Give the position of every Plasmodium falciparum parasite, noting its life-cycle stage.
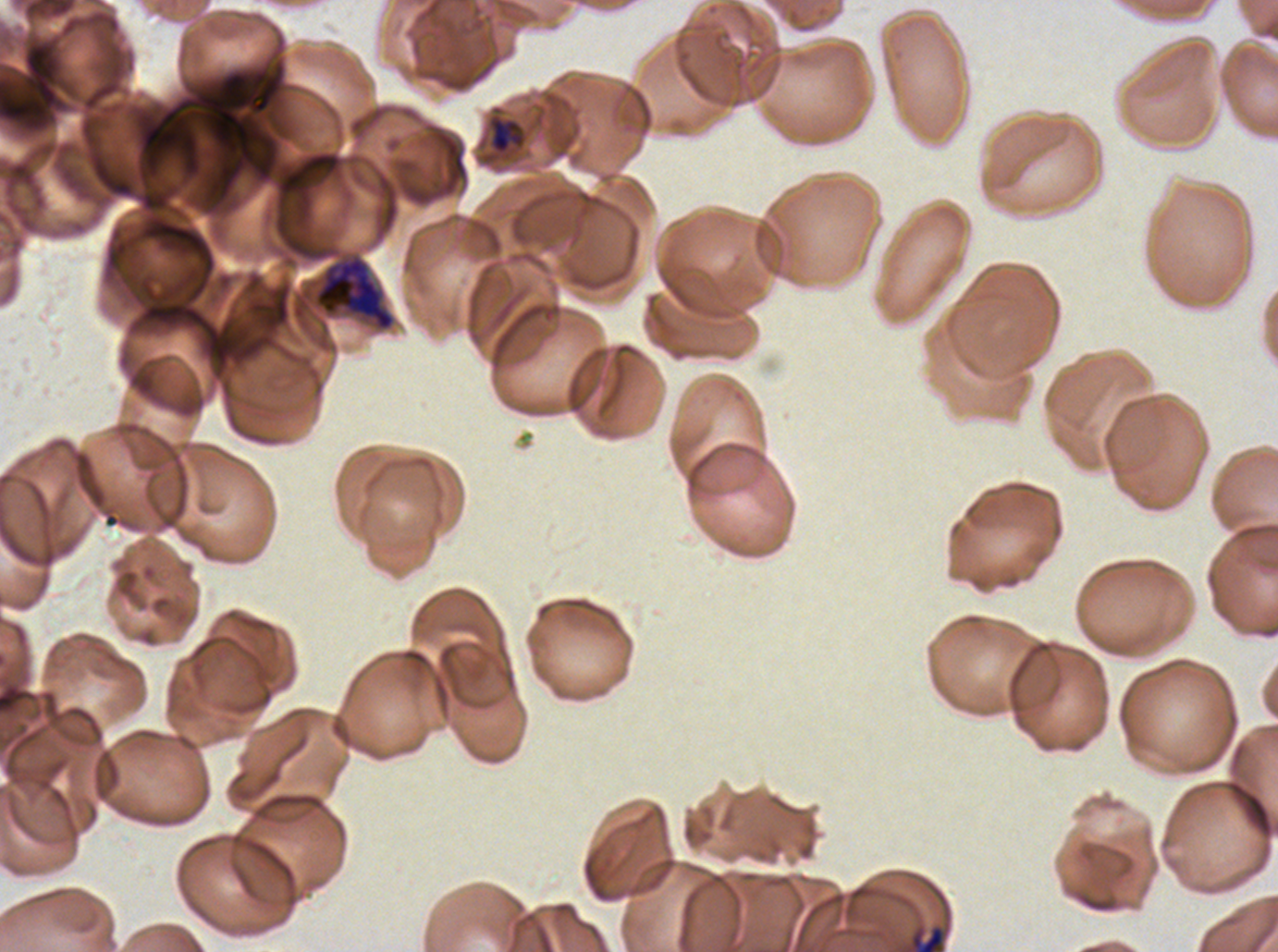

Approximate bounding boxes as [x1, y1, x2, y2] in pixels.
Late-ring/early-trophozoite forms: [909, 924, 945, 951].
Late trophozoites: [490, 117, 524, 154].
Early schizonts: [312, 252, 396, 332].
No rings, mid trophozoites, late schizonts, segmenters, or gametocytes observed.

Image is 1278×952 pixels. Ex-vivo Plasmodium falciparum culture from a patient in The Gambia, grown for 24 to 48 hours. Thin blood smear. Life-cycle stages observed: late-ring/early-trophozoite, late trophozoite, early schizont. A sub-image separated from a larger composite. Giemsa-stained preparation.